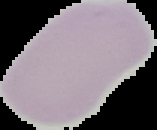

Summary:
  - Result: no malaria parasites detected
  - Preparation: thin blood smear
  - Image size: 157×130 pixels
  - Image type: segmented cell region with the area outside set to black